Give the position of every Plasmodium parasite.
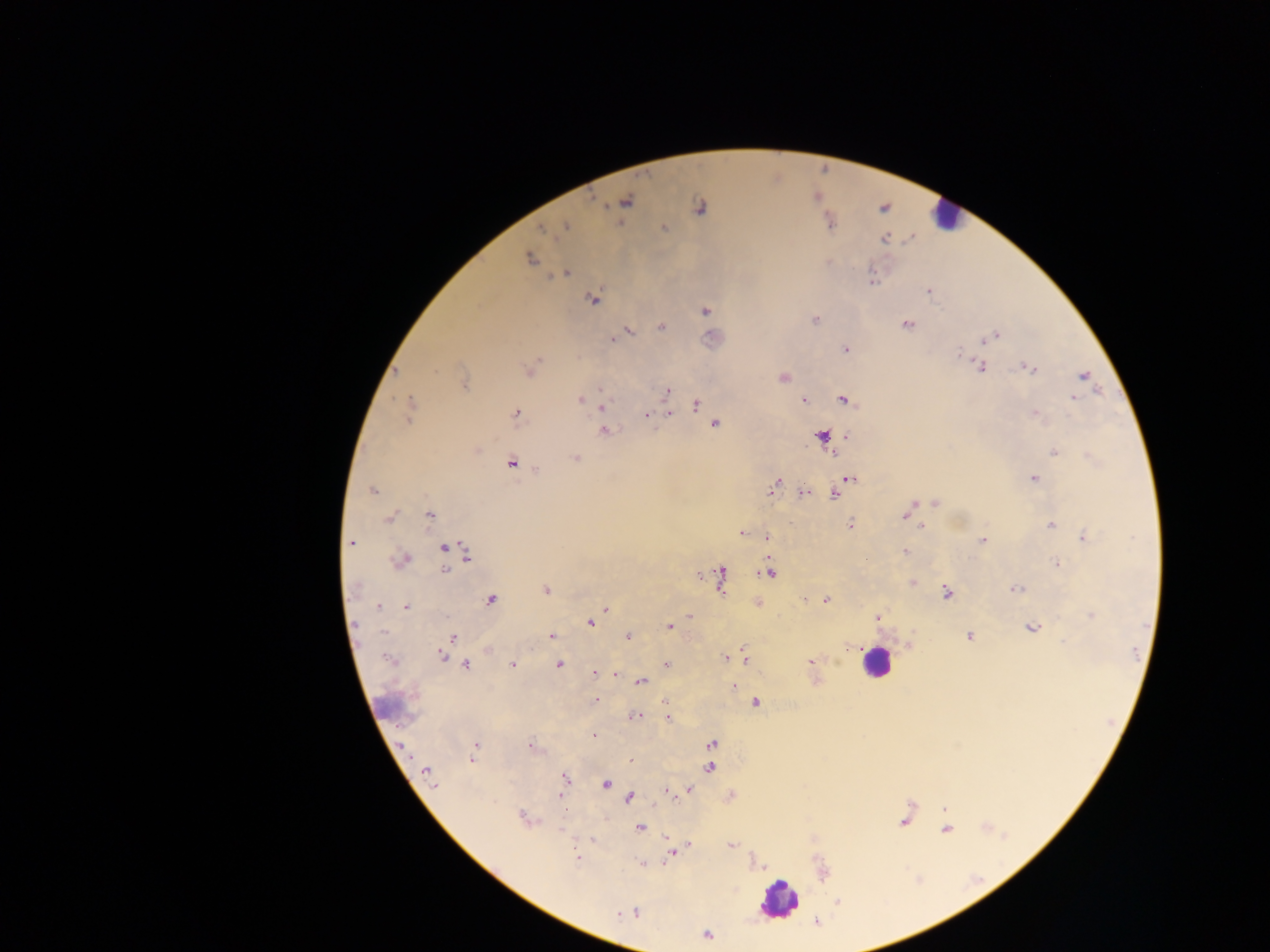
Approximate centers as {x, y} in pixels.
Plasmodium parasites: {625, 201}, {699, 208}, {829, 221}, {566, 227}, {663, 227}, {543, 229}, {884, 238}, {530, 258}, {567, 272}, {871, 281}, {928, 291}, {593, 299}, {705, 310}, {814, 319}, {906, 325}, {660, 327}, {628, 330}, {620, 335}, {995, 336}, {613, 339}, {845, 350}, {959, 352}, {979, 366}, {1028, 368}, {530, 369}, {782, 376}, {1083, 376}, {463, 382}, {667, 390}, {1073, 397}, {581, 399}, {843, 399}, {804, 400}, {586, 401}, {696, 404}, {668, 405}, {601, 406}, {410, 409}, {515, 413}, {1035, 413}, {647, 414}, {669, 414}, {715, 423}, {603, 430}, {821, 436}, {846, 436}, {475, 450}, {1053, 451}, {832, 452}, {575, 458}, {512, 463}, {1034, 478}, {849, 479}, {774, 486}, {372, 490}, {803, 493}, {835, 494}, {935, 502}, {909, 509}, {429, 515}, {389, 516}, {849, 524}, {1050, 525}, {921, 527}, {740, 533}, {766, 537}, {1083, 537}, {982, 540}, {351, 543}, {445, 548}, {451, 549}, {904, 551}, {465, 554}, {400, 560}, {1058, 564}, {768, 571}, {720, 578}, {911, 582}, {546, 589}, {1015, 589}, {946, 592}, {826, 599}, {491, 600}, {757, 603}, {376, 605}, {407, 606}, {605, 607}, {689, 615}, {1091, 615}, {876, 616}, {590, 622}, {669, 627}, {1031, 627}, {551, 635}, {969, 635}, {453, 636}, {628, 636}, {909, 645}, {489, 649}, {442, 655}, {446, 656}, {744, 657}, {725, 658}, {390, 660}, {811, 661}, {512, 664}, {665, 664}, {464, 665}, {558, 665}, {594, 673}, {615, 674}, {625, 677}, {640, 682}, {733, 687}, {597, 700}, {665, 701}, {757, 702}, {634, 716}, {667, 718}, {592, 735}, {711, 743}, {531, 746}, {476, 747}, {472, 756}, {629, 759}, {710, 767}, {427, 774}, {564, 778}, {605, 783}, {686, 789}, {666, 792}, {730, 795}, {561, 796}, {629, 797}, {943, 809}, {523, 818}, {904, 821}, {639, 828}, {946, 829}, {592, 839}, {731, 845}, {688, 846}, {671, 853}, {577, 858}, {643, 864}, {762, 866}, {634, 912}, {621, 913}, {630, 913}, {816, 921}, {706, 935}.

capture = mobile-phone photograph through a microscope
image size = 1270×952 pixels
field of view = single
leukocyte locations = approximate centers as {x, y} in pixels: {945, 216}, {876, 661}, {778, 900}
preparation = thick blood smear
country = Ghana